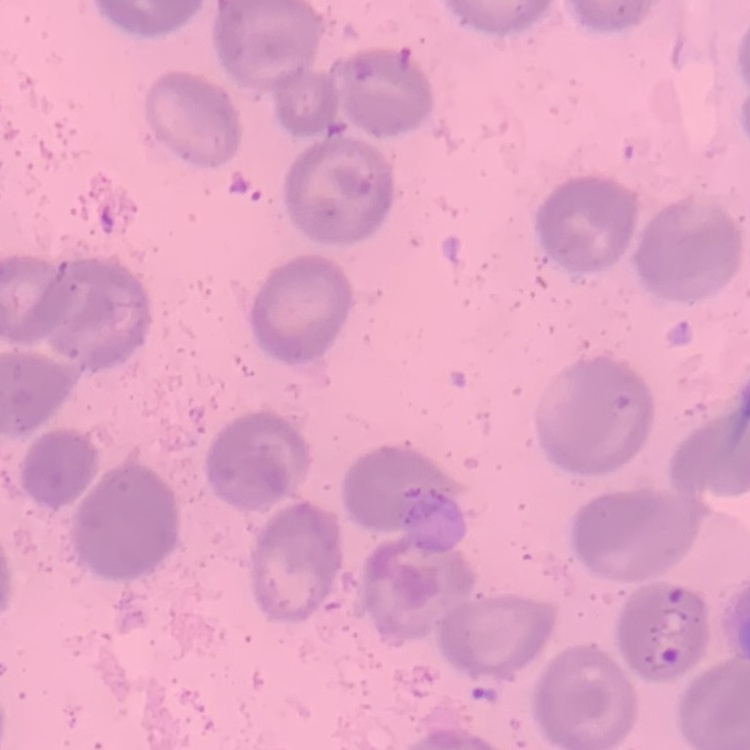

The red blood cells exhibit no rouleaux formation. Field's or Giemsa stain. Thin blood smear. Square crop of a larger photomicrograph.